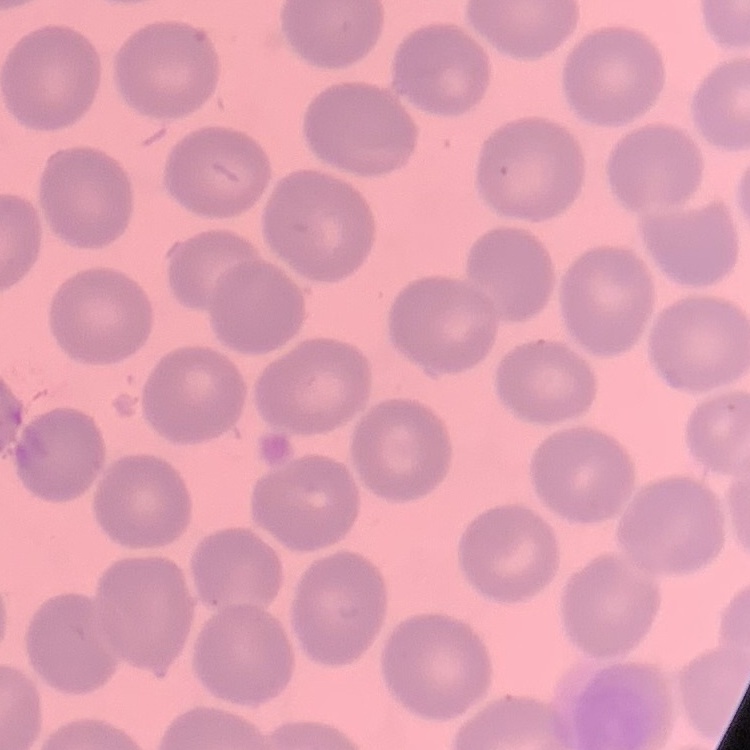
Summary:
  - Erythrocyte morphology: no rouleaux formation
  - Preparation: thin blood film
  - Image type: square crop of a larger photomicrograph
  - Stain: Field's or Giemsa